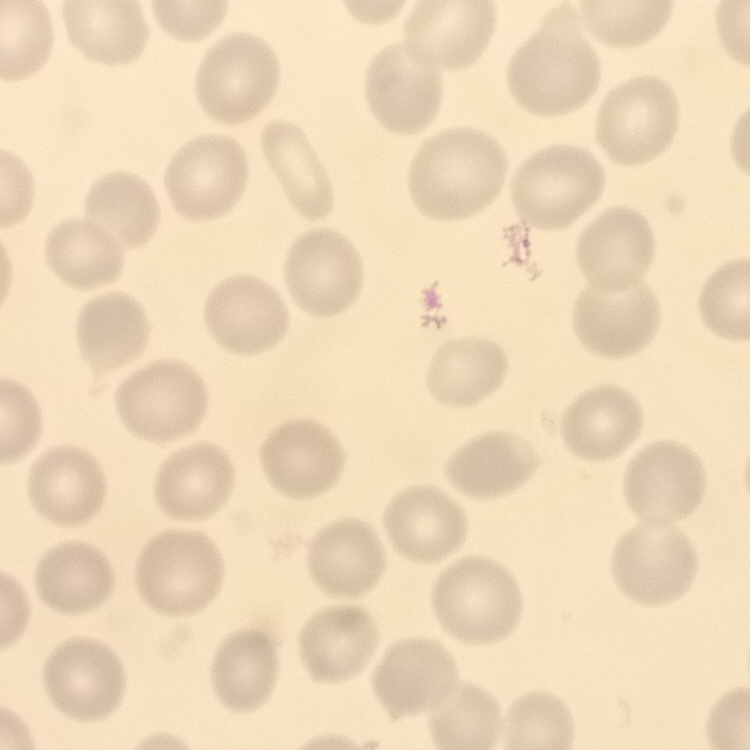
erythrocyte_morphology: no rouleaux formation
preparation: thin blood smear
stain: Field's or Giemsa
image_type: one tile cut from a larger photomicrograph